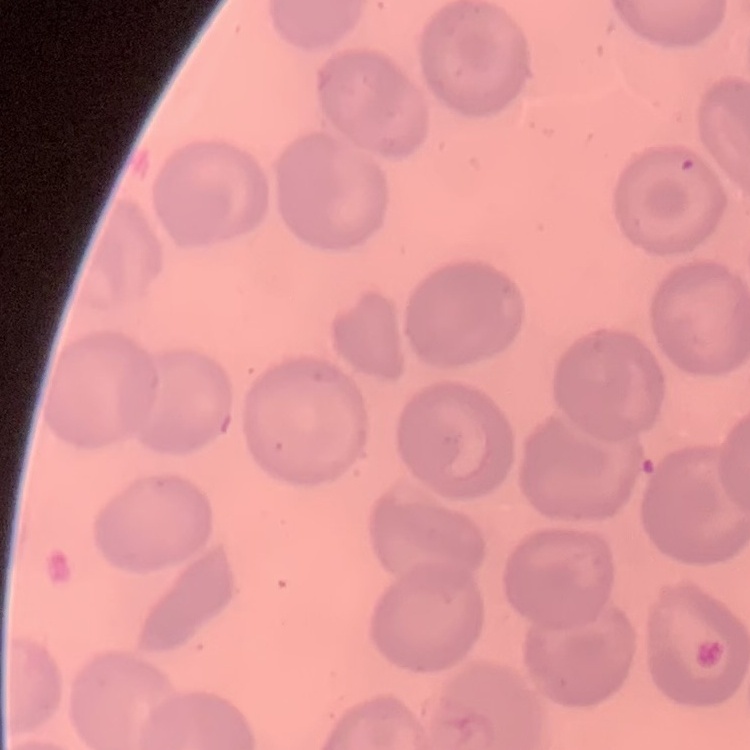
The erythrocytes show no rouleaux formation. Square crop of a larger photomicrograph. Field's or Giemsa stain. Thin blood smear.